Give the extent of all uninfected red blood cells.
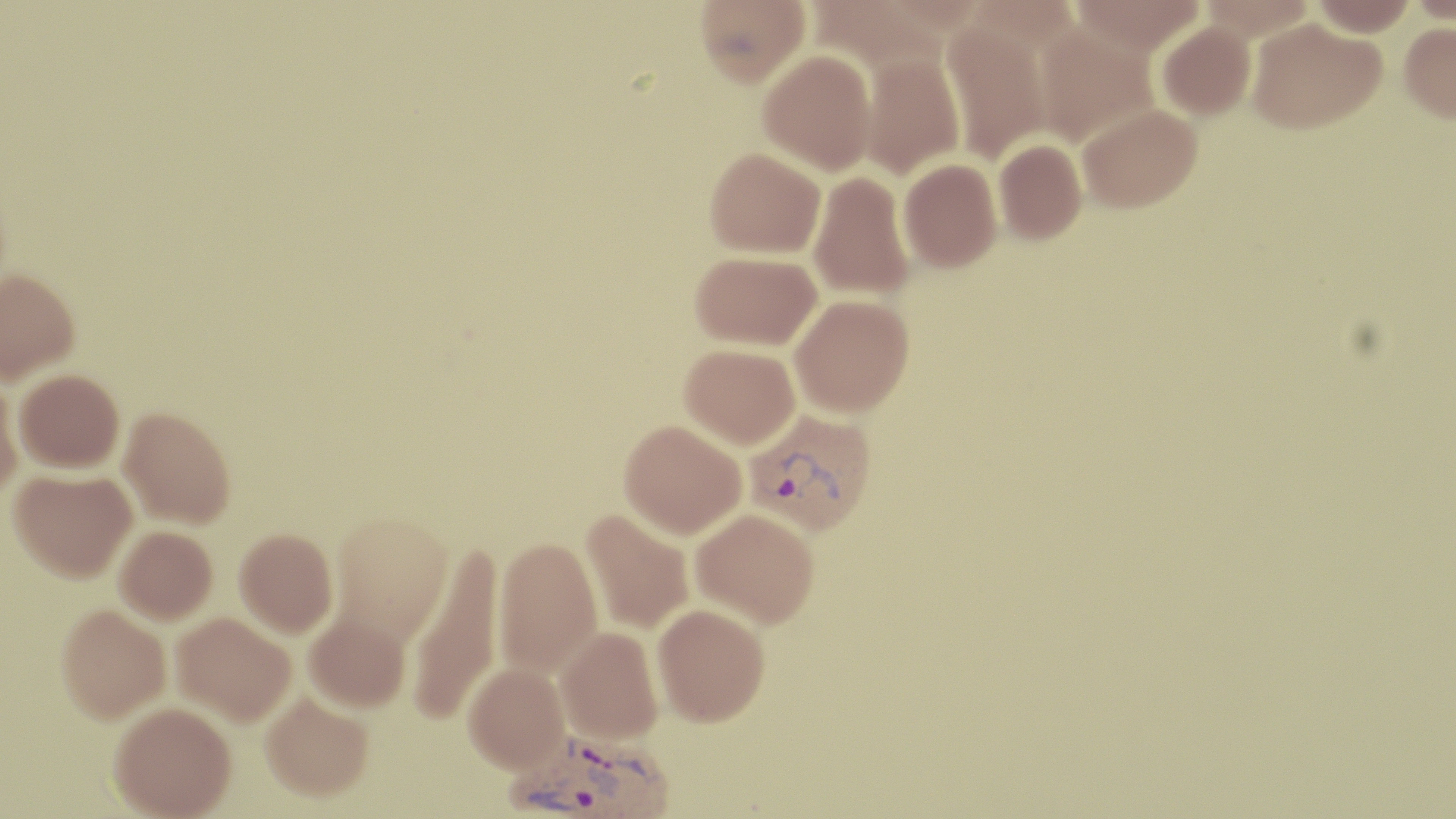
Approximate bounding boxes as [x1, y1, x2, y2] in pixels.
Uninfected red blood cells: [695, 0, 809, 86], [1068, 0, 1206, 56], [1310, 0, 1417, 35], [942, 18, 1050, 164], [1247, 18, 1384, 134], [1033, 21, 1158, 147], [1157, 21, 1256, 120], [1399, 22, 1456, 121], [757, 50, 876, 175], [859, 52, 965, 179], [1077, 103, 1203, 213], [994, 139, 1087, 244], [705, 147, 825, 258], [898, 159, 1002, 272], [808, 171, 915, 301], [691, 251, 822, 349], [0, 273, 80, 387], [790, 294, 914, 418], [680, 344, 800, 450], [14, 374, 124, 477], [0, 381, 23, 503], [118, 411, 235, 532], [619, 422, 747, 541], [9, 473, 137, 588], [691, 508, 819, 630], [580, 510, 693, 634], [330, 515, 454, 648], [114, 529, 217, 627], [234, 533, 337, 641], [493, 540, 603, 681], [408, 546, 504, 727], [653, 606, 770, 731], [56, 610, 170, 729], [304, 615, 411, 714], [171, 617, 295, 730], [556, 629, 663, 747], [463, 667, 570, 779], [261, 698, 374, 806], [108, 708, 236, 819].

Summary:
  - Plasmodium vivax-infected red blood cell locations: [744, 409, 877, 537], [504, 732, 677, 819]
  - Slide-level diagnosis: Plasmodium vivax
  - Magnification: 1000x
  - Modality: light microscopy
  - Field of view: single
  - Image size: 1456×819 pixels
  - Preparation: thin blood film
  - Stain: May-Grünwald-Giemsa